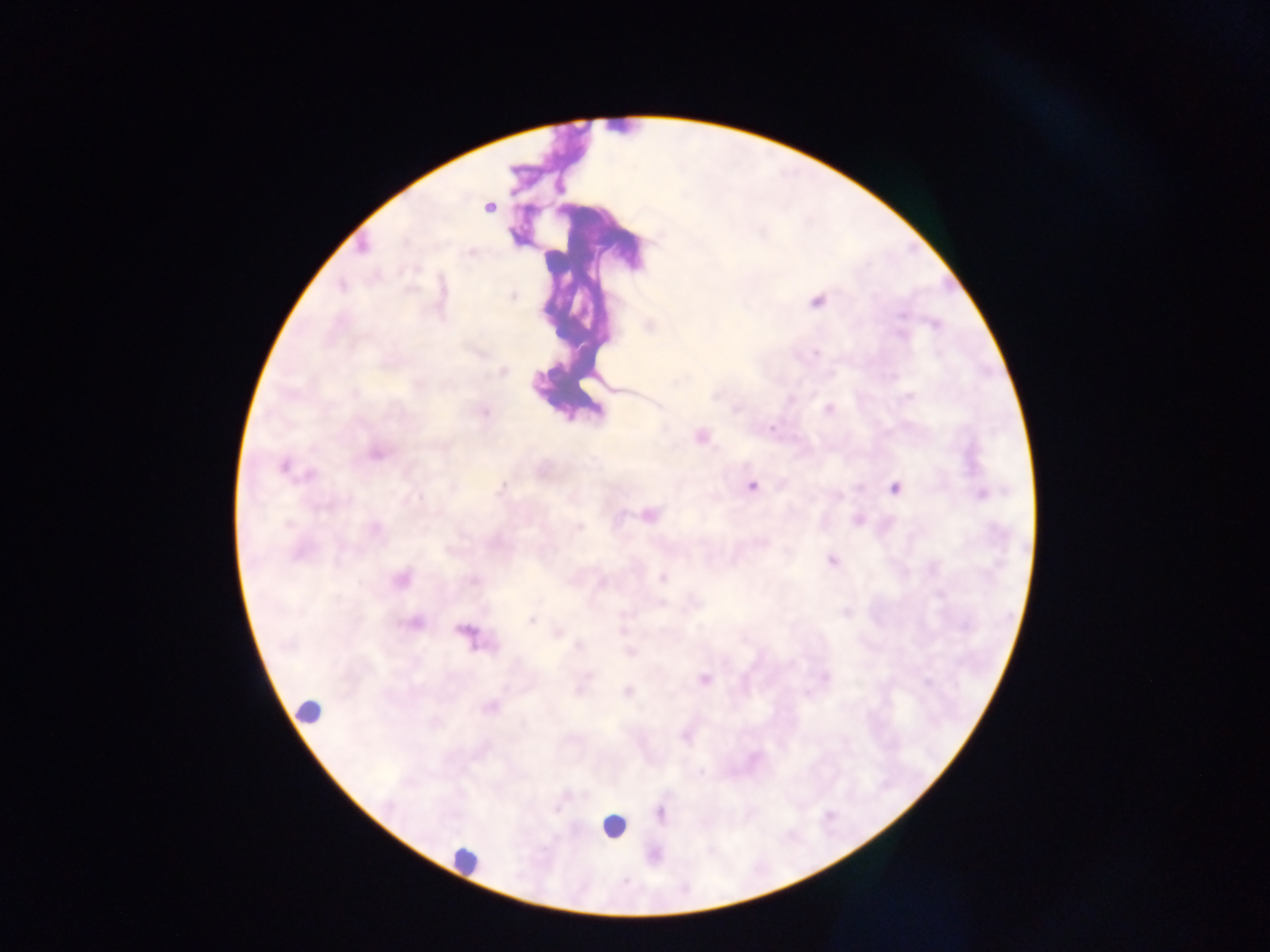
Approximate centers as [x, y] in pixels.
Summary:
  - Malaria parasite locations: [489, 208], [362, 247], [471, 254], [416, 268], [342, 287], [513, 295], [817, 302], [901, 315], [935, 324], [901, 335], [815, 353], [503, 371], [893, 377], [678, 381], [354, 392], [716, 396], [909, 397], [736, 409], [829, 409], [485, 413], [771, 428], [700, 436], [376, 454], [283, 467], [311, 475], [502, 486], [751, 486], [895, 487], [454, 488], [981, 494], [416, 499], [650, 515], [288, 524], [579, 526], [376, 529], [761, 542], [831, 561], [662, 577], [401, 579], [474, 580], [661, 604], [531, 620], [415, 623], [465, 631], [558, 634], [579, 644], [631, 652], [588, 675], [826, 677], [704, 679], [927, 683], [628, 691], [491, 707]
  - Leukocyte locations: [309, 711], [613, 825], [464, 859]
  - Country: Ghana
  - Image size: 1270×952 pixels
  - Preparation: thick blood smear
  - Field of view: single
  - Capture: mobile-phone photograph through a microscope